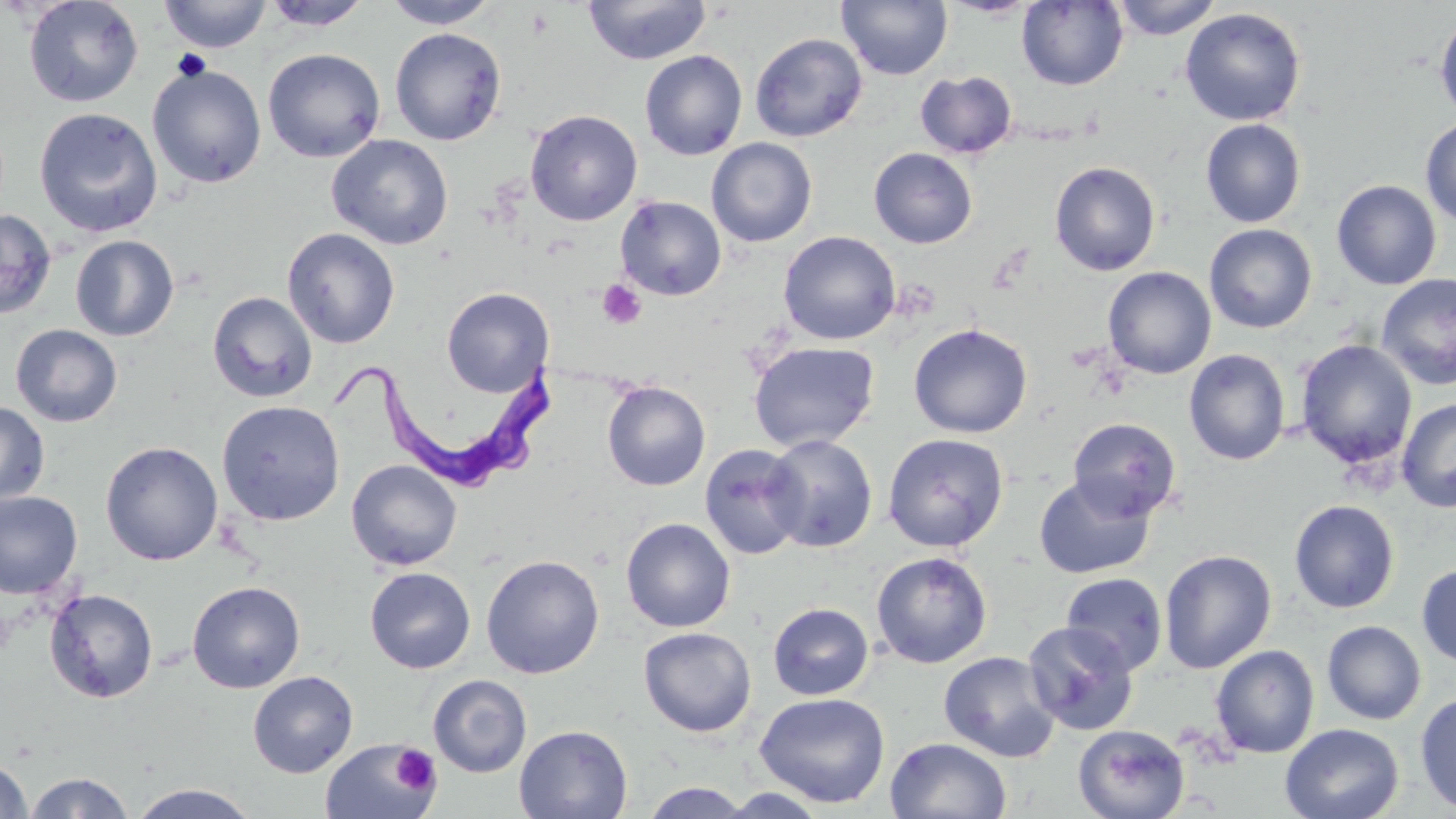

Summary:
  - Coordinate format: approximate bounding boxes as (x1, y1, x2, y2) in pixels
  - Trypanosoma brucei locations: (334, 352, 567, 490)
  - Uninfected red blood cell locations: (23, 0, 144, 107), (159, 0, 272, 53), (382, 0, 499, 28), (837, 0, 952, 80), (1017, 0, 1128, 90), (1110, 0, 1222, 40), (260, 1, 372, 31), (583, 1, 712, 65), (1179, 8, 1306, 126), (1434, 13, 1456, 123), (390, 27, 507, 145), (750, 32, 867, 142), (262, 48, 385, 162), (639, 50, 748, 160), (147, 63, 266, 188), (915, 69, 1017, 159), (34, 107, 163, 237), (524, 109, 643, 226), (1200, 118, 1306, 228), (1420, 118, 1456, 228), (327, 134, 453, 249), (707, 137, 818, 247), (869, 147, 977, 248), (1049, 161, 1161, 276), (1332, 179, 1442, 290), (615, 195, 726, 301), (0, 208, 56, 320), (1204, 223, 1317, 333), (282, 227, 400, 348), (778, 231, 901, 345), (70, 235, 179, 341), (1102, 266, 1216, 379), (1376, 273, 1456, 391), (441, 287, 554, 397), (207, 291, 318, 403), (908, 323, 1033, 438), (10, 324, 122, 427), (1295, 339, 1418, 469), (748, 341, 880, 452), (1184, 349, 1291, 466), (602, 381, 710, 491), (1396, 398, 1456, 512), (216, 399, 345, 526), (0, 401, 50, 506), (1068, 417, 1182, 521), (882, 432, 1009, 552), (764, 435, 878, 553), (101, 441, 223, 566), (699, 444, 807, 560), (346, 459, 463, 570), (1033, 474, 1156, 580), (0, 491, 83, 600), (1289, 499, 1400, 613), (621, 517, 736, 632), (1159, 549, 1277, 673), (871, 551, 992, 668), (482, 554, 604, 678), (1416, 562, 1456, 669), (365, 567, 476, 673), (1061, 572, 1167, 675), (187, 581, 305, 693), (44, 588, 159, 703), (768, 602, 874, 700), (1022, 620, 1139, 735), (1322, 620, 1426, 724), (639, 627, 756, 737), (1210, 644, 1319, 758), (939, 651, 1061, 762), (248, 670, 358, 777), (428, 674, 531, 777), (754, 692, 890, 808), (1414, 692, 1456, 815), (1280, 723, 1404, 819), (514, 724, 633, 819), (1073, 725, 1189, 819), (885, 736, 1012, 819), (321, 738, 439, 819), (0, 757, 33, 819), (22, 771, 134, 818), (639, 782, 756, 817), (129, 783, 260, 819), (714, 788, 832, 818)
  - Platelet locations: (526, 6, 555, 39), (598, 280, 646, 329), (391, 745, 439, 794)
  - Slide-level diagnosis: Trypanosoma brucei
  - Image size: 1456×819 pixels
  - Field of view: single
  - Modality: light microscopy
  - Magnification: 1000x
  - Preparation: thin blood film
  - Stain: May-Grünwald-Giemsa